Assess this cell for malaria.
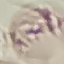

Uninfected.

Thin blood smear. Giemsa stain. Acquired by smartphone through the microscope eyepiece. Automatically extracted cell patch, resized to 64 × 64 pixels.